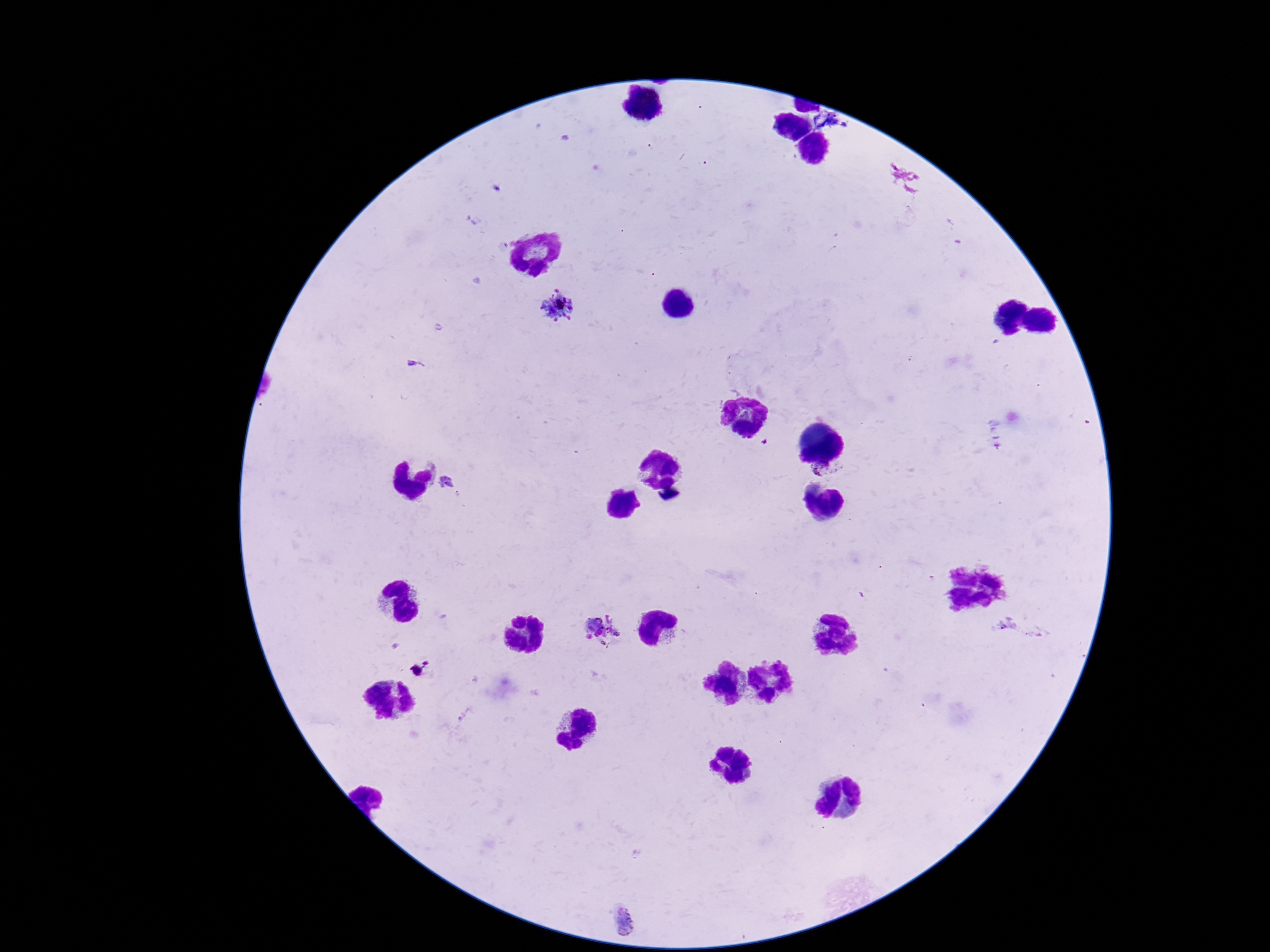
stain = Giemsa
Plasmodium parasite locations = approximate centers as [x, y] in pixels: [559, 307], [829, 470], [446, 483], [600, 632], [626, 920]
patient malaria status = infected
capture = smartphone camera through the microscope eyepiece
magnification = 100x
field of view = single
image size = 1270×952 pixels
preparation = thick blood smear